Assess this cell for malaria.
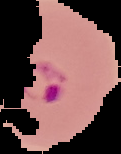
Parasitized.

image type = segmented cell region with the area outside set to black
preparation = thin blood film
image size = 121×154 pixels